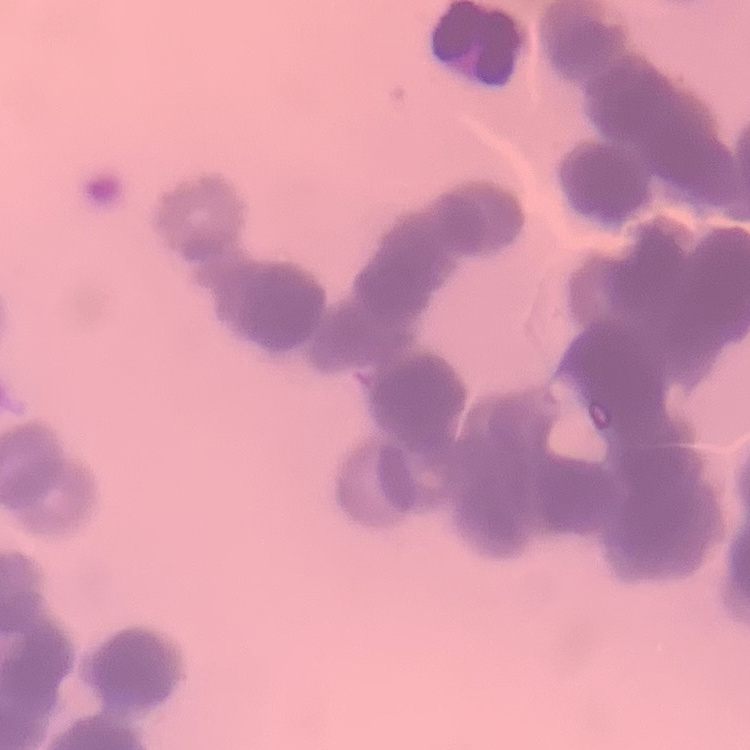
red blood cell morphology = rouleaux formation
stain = Field's or Giemsa
preparation = thin blood film
image type = one tile cut from a larger photomicrograph